Look for Plasmodium parasites.
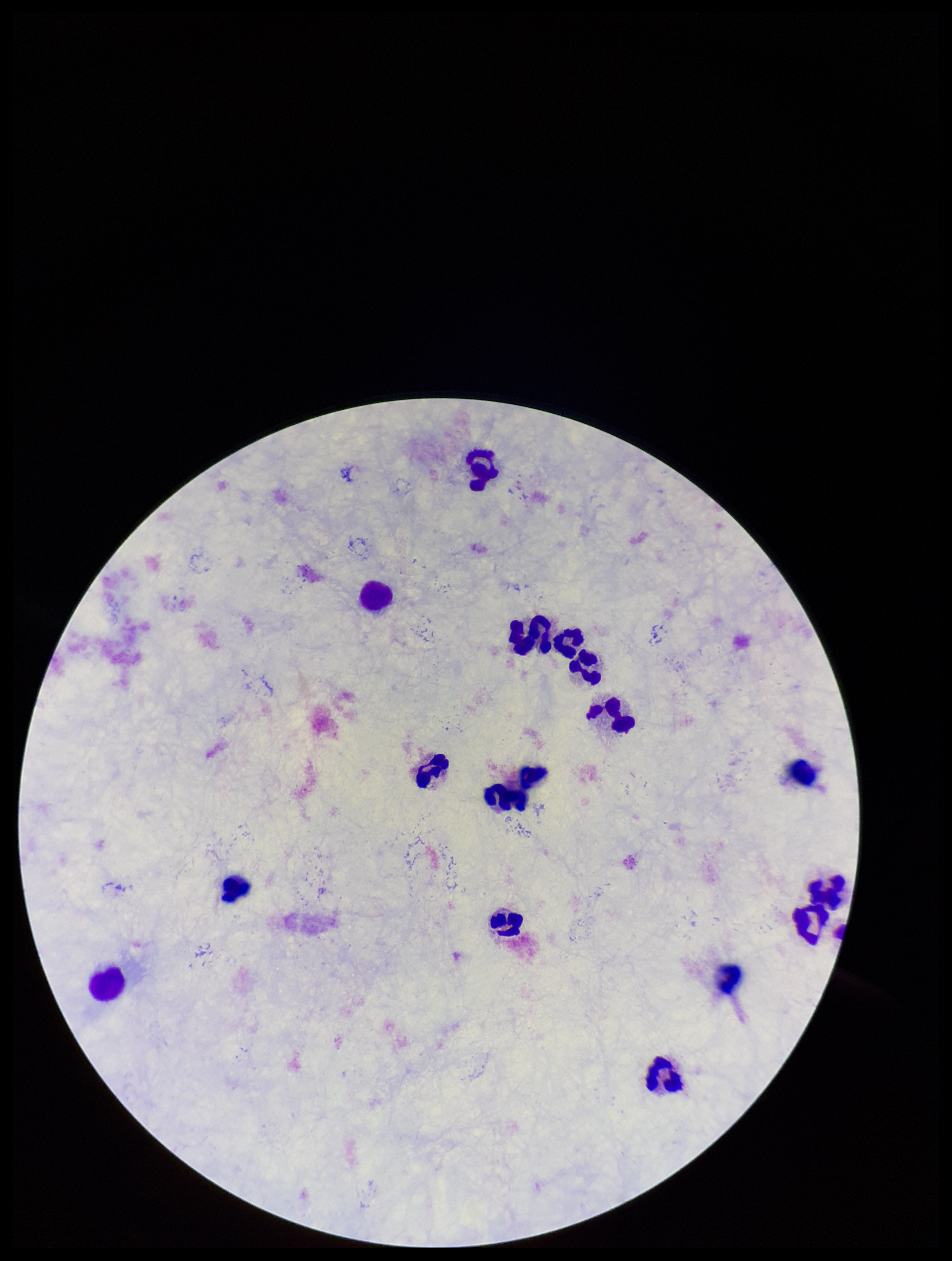
None seen.

leukocyte_count: 15
image_size: 952×1261 pixels
preparation: thick smear
parasite_count: 0
capture: smartphone photograph through the microscope eyepiece
stain: Giemsa
patient_malaria_status: negative
field_of_view: one from this slide